Comment on the morphology of the red blood cells.
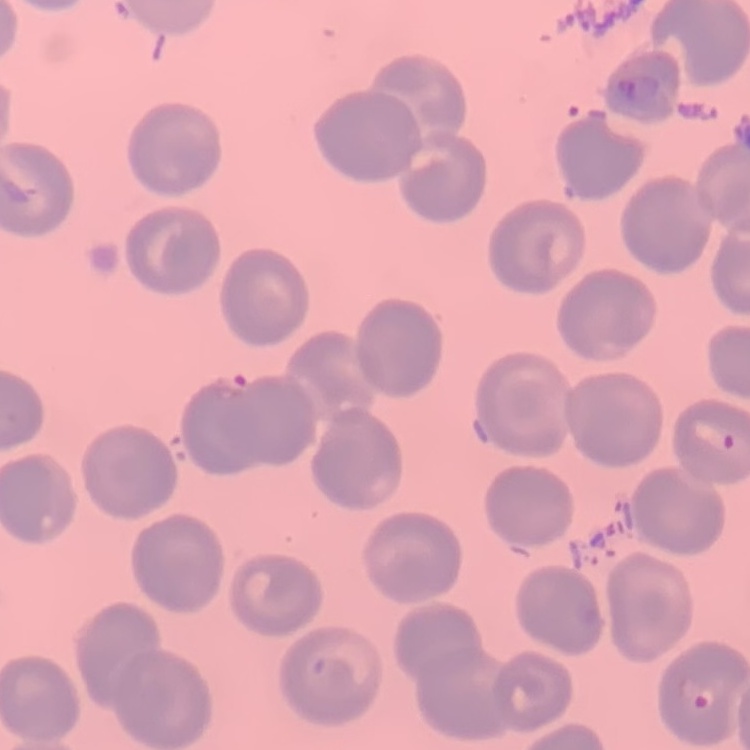
No rouleaux formation.

One tile cut from a larger photomicrograph. Thin blood film. Stained with either Field's or Giemsa.